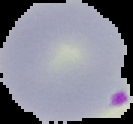

Summary:
  - Image type: cell region segmented out of the field of view; surrounding area masked to black
  - Image size: 133×124 pixels
  - Preparation: thin blood smear
  - Result: malaria parasites detected